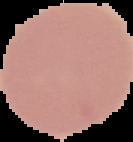
Malaria status: uninfected. Segmented cell region on a black background. From a thin blood smear. Image is 133×142 pixels.